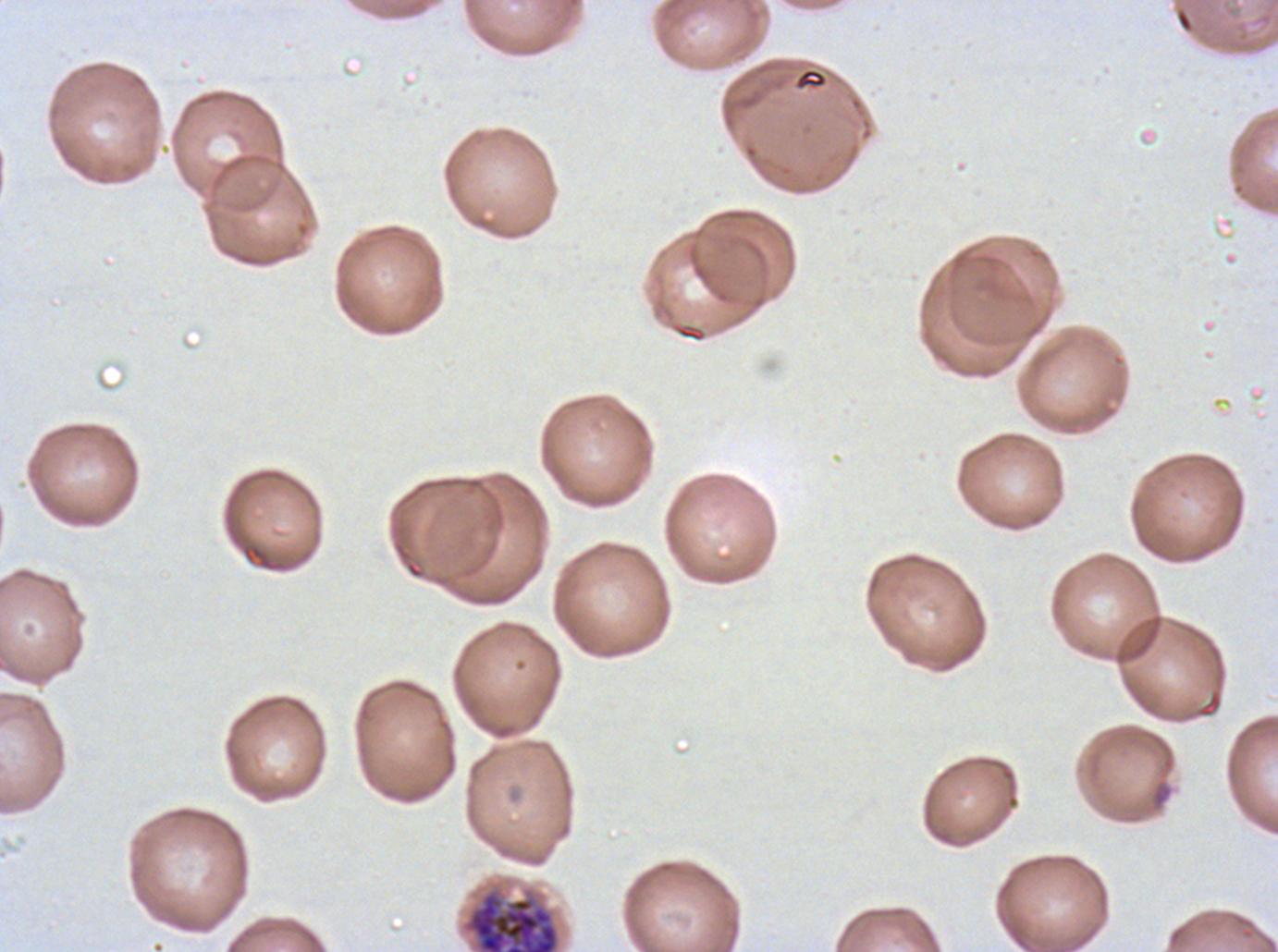

notation = approximate bounding boxes as (x1, y1, x2, y2) in pixels
early schizont locations = (462, 888, 560, 951)
specimen = P. falciparum from a patient in The Gambia, cultured ex vivo for 24 to 48 hours
stain = Giemsa
image size = 1278×952 pixels
field of view = one sub-image of a larger composite
preparation = thin blood film